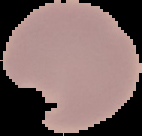

Result: Plasmodium parasites identified. The area outside the segmented cell region is set to black. From a thin blood smear. Image is 142×136 pixels.